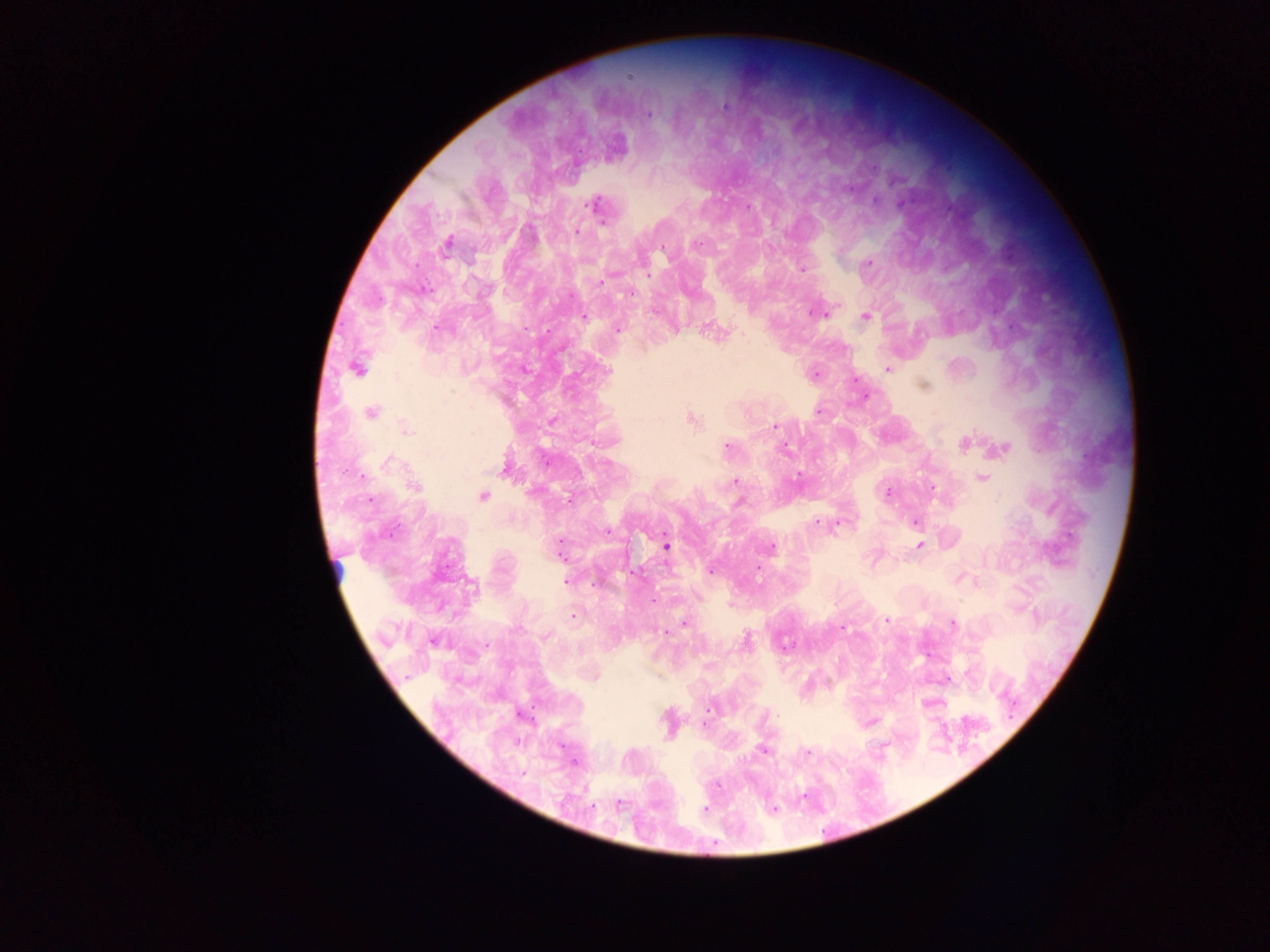

Approximate centers as {x, y} in pixels. Plasmodium parasite locations: {629, 78}, {725, 106}, {649, 114}, {879, 201}, {899, 203}, {597, 208}, {576, 232}, {447, 242}, {866, 263}, {802, 267}, {602, 280}, {812, 311}, {818, 314}, {830, 314}, {866, 314}, {582, 316}, {356, 369}, {886, 369}, {923, 385}, {453, 392}, {865, 396}, {370, 413}, {691, 419}, {771, 424}, {404, 428}, {964, 442}, {728, 448}, {1005, 448}, {786, 450}, {390, 462}, {361, 475}, {798, 476}, {733, 479}, {981, 479}, {414, 487}, {889, 493}, {483, 497}, {566, 498}, {737, 501}, {916, 521}, {817, 522}, {606, 531}, {918, 544}, {667, 546}, {771, 548}, {756, 572}, {567, 580}, {573, 614}, {885, 620}, {954, 623}, {684, 624}, {844, 626}, {545, 637}, {433, 639}, {746, 640}, {830, 685}, {925, 705}, {764, 751}, {810, 753}, {576, 762}, {619, 805}, {772, 806}, {704, 807}. Thick blood film. Collected in Ghana. Photographed through a microscope with a mobile-phone camera. Image is 1270×952 pixels. One field of view.